Assess this cell for malaria.
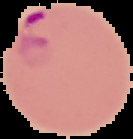

Parasitized.

Image is 133×139 pixels. The area outside the segmented cell region is set to black. From a thin blood film.